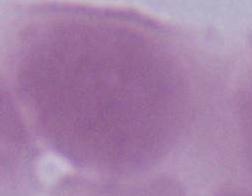

identification: erythrocyte
magnification: 1000x
modality: micrograph